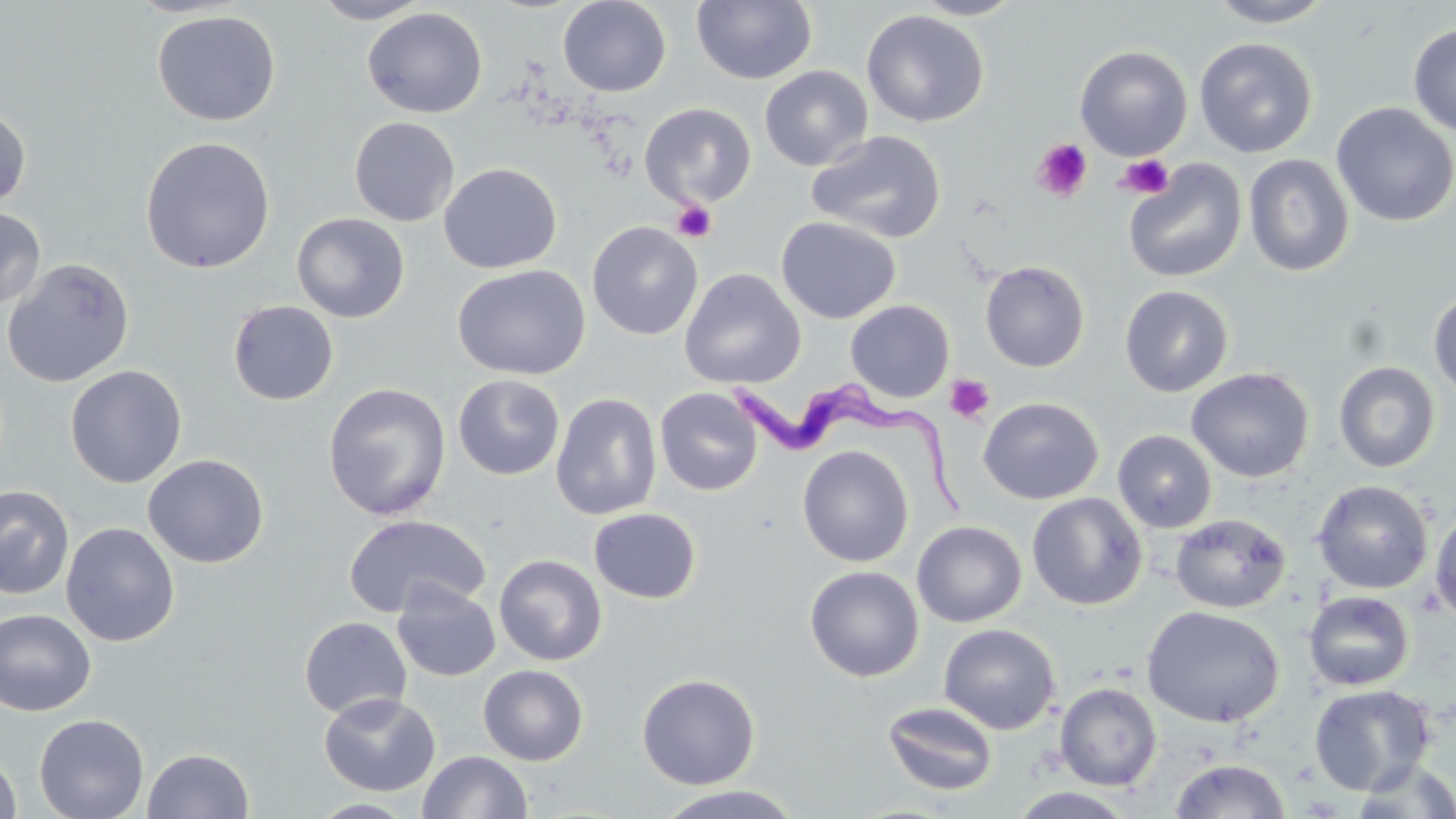

Summary:
  - Coordinate format: approximate bounding boxes as (x1, y1, x2, y2) in pixels
  - Uninfected red blood cell locations: (311, 0, 432, 24), (558, 0, 672, 97), (910, 0, 1027, 20), (1204, 0, 1338, 28), (691, 1, 817, 85), (362, 7, 488, 118), (152, 10, 281, 126), (861, 10, 990, 127), (1408, 23, 1456, 138), (1194, 37, 1318, 159), (1075, 44, 1192, 161), (759, 65, 873, 171), (1331, 102, 1456, 227), (639, 103, 756, 207), (0, 106, 31, 210), (349, 116, 460, 226), (807, 130, 947, 243), (139, 136, 276, 274), (1243, 154, 1355, 277), (1123, 159, 1246, 284), (438, 163, 563, 274), (0, 207, 46, 309), (291, 212, 410, 323), (776, 216, 901, 324), (587, 221, 703, 340), (1, 258, 135, 387), (980, 260, 1090, 372), (452, 265, 590, 380), (679, 268, 806, 389), (1119, 285, 1234, 397), (1427, 290, 1456, 399), (228, 300, 339, 406), (845, 300, 955, 402), (1333, 361, 1440, 473), (65, 365, 187, 488), (1185, 367, 1315, 483), (453, 374, 565, 480), (322, 382, 451, 520), (655, 387, 763, 496), (550, 393, 662, 521), (977, 396, 1103, 505), (1112, 429, 1217, 533), (796, 445, 914, 567), (143, 454, 269, 569), (1312, 480, 1433, 595), (0, 485, 75, 600), (1026, 492, 1148, 610), (1429, 503, 1456, 624), (588, 508, 702, 604), (1170, 513, 1291, 614), (343, 514, 490, 618), (912, 520, 1026, 627), (61, 522, 180, 647), (494, 554, 607, 666), (804, 565, 924, 682), (392, 583, 501, 682), (1303, 591, 1414, 692), (1141, 606, 1285, 728), (0, 608, 96, 716), (298, 616, 412, 719), (938, 623, 1061, 735), (477, 664, 589, 766), (636, 672, 761, 790), (1055, 683, 1162, 790), (1308, 683, 1437, 795), (319, 691, 440, 797), (882, 700, 998, 797), (34, 713, 149, 819), (143, 748, 254, 819), (0, 749, 22, 819), (417, 750, 532, 818), (1168, 757, 1291, 818), (1350, 759, 1456, 818), (654, 785, 805, 819), (1007, 787, 1138, 818), (309, 798, 420, 817)
  - Platelet locations: (1032, 138, 1093, 202), (1116, 154, 1175, 200), (671, 199, 716, 242), (945, 374, 995, 424)
  - Trypanosoma brucei locations: (728, 379, 969, 518)
  - Slide-level diagnosis: Trypanosoma brucei
  - Magnification: 1000x
  - Image size: 1456×819 pixels
  - Modality: optical microscopy
  - Field of view: one of a larger specimen
  - Stain: May-Grünwald-Giemsa
  - Preparation: thin blood smear